Locate every uninfected red blood cell.
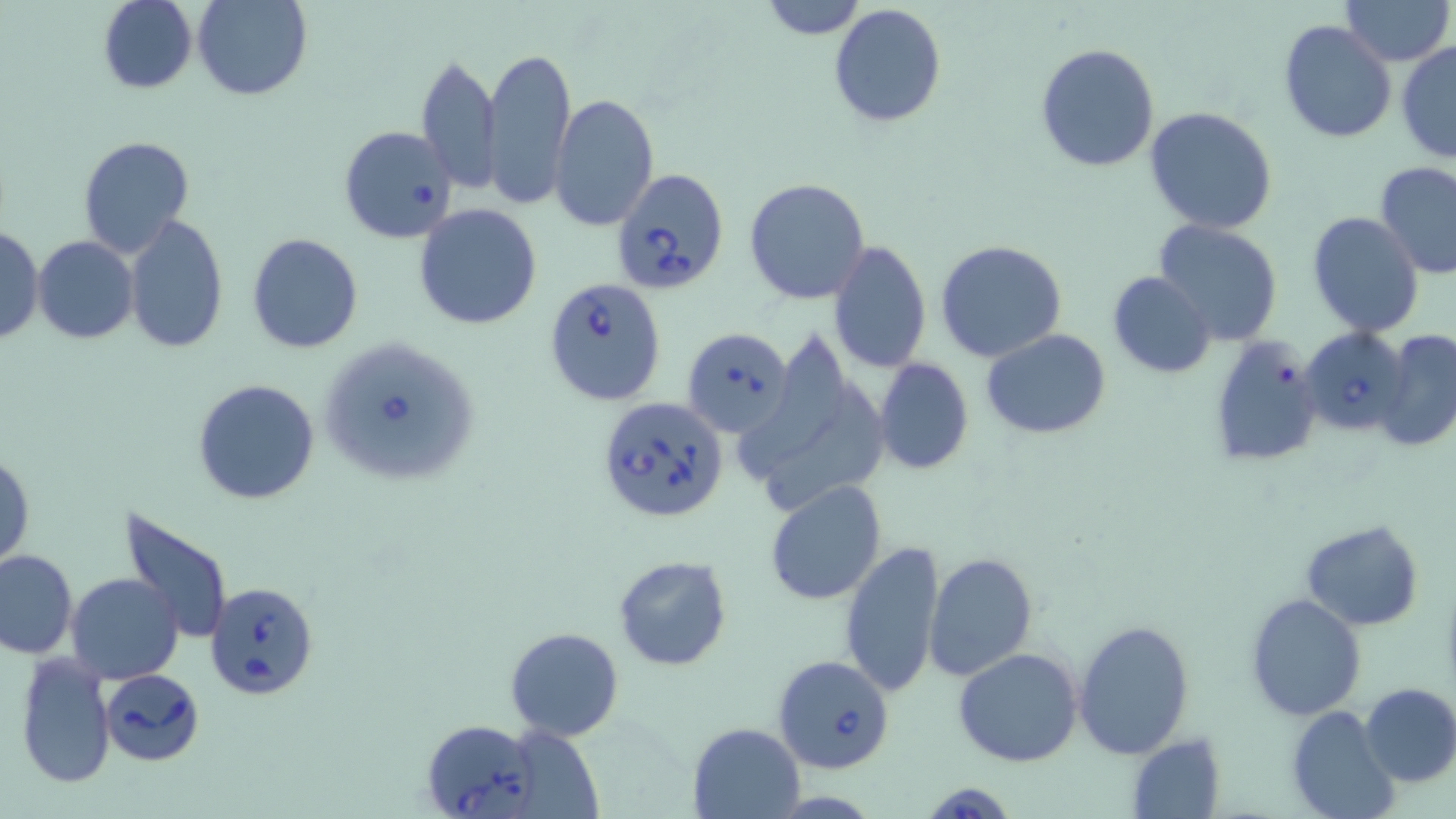
Approximate bounding boxes as [x1, y1, x2, y2] in pixels.
Uninfected red blood cells: [97, 0, 197, 94], [193, 0, 311, 100], [757, 0, 869, 39], [1341, 0, 1453, 66], [828, 4, 948, 129], [1279, 19, 1398, 145], [1395, 42, 1456, 164], [1035, 43, 1160, 173], [482, 44, 576, 210], [416, 54, 502, 194], [550, 92, 660, 232], [1144, 105, 1278, 233], [77, 136, 194, 256], [1373, 160, 1456, 280], [744, 177, 870, 304], [413, 203, 544, 330], [1306, 211, 1426, 338], [122, 216, 230, 354], [1154, 219, 1284, 346], [0, 226, 43, 345], [247, 233, 363, 353], [33, 236, 139, 344], [935, 239, 1066, 362], [828, 241, 932, 374], [1107, 270, 1215, 378], [981, 328, 1112, 439], [1374, 328, 1456, 455], [1206, 336, 1323, 468], [739, 338, 847, 477], [874, 358, 974, 475], [192, 378, 321, 506], [765, 381, 887, 508], [1, 453, 34, 569], [765, 480, 888, 605], [116, 507, 236, 647], [1301, 519, 1426, 631], [839, 538, 945, 701], [1, 549, 77, 659], [924, 552, 1036, 683], [613, 555, 732, 672], [66, 573, 184, 684], [1244, 592, 1366, 721], [1074, 617, 1196, 758], [505, 627, 624, 742], [953, 648, 1083, 768], [12, 654, 116, 790], [1358, 682, 1456, 787], [1287, 707, 1400, 819], [687, 721, 804, 817], [1125, 733, 1227, 819].

slide-level diagnosis = Babesia divergens
stain = May-Grünwald-Giemsa
preparation = thin blood smear
image size = 1456×819 pixels
modality = optical microscopy
Babesia divergens-infected red blood cell locations = approximate bounding boxes as [x1, y1, x2, y2] in pixels: [338, 126, 458, 245], [611, 169, 730, 295], [545, 281, 663, 404], [1299, 324, 1413, 437], [681, 327, 793, 435], [318, 336, 484, 487], [597, 395, 729, 525], [205, 580, 319, 701], [771, 654, 895, 773], [99, 669, 205, 766], [421, 719, 542, 819], [920, 780, 1020, 819]
magnification = 1000x
field of view = one of a larger specimen